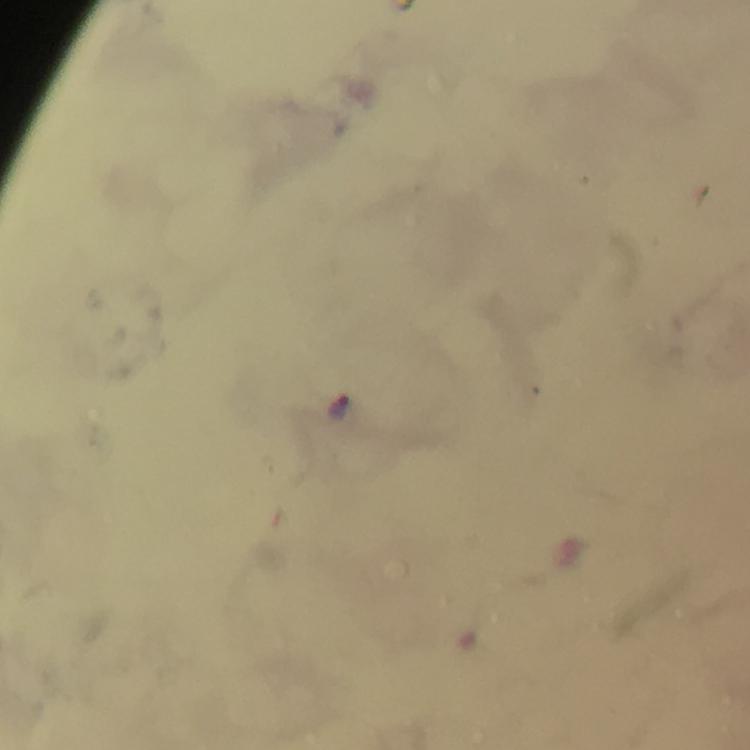

Approximate centers as [x, y] in pixels. Plasmodium parasite locations: [341, 405]. Cropped region of a single field of view. 100x magnification. Thick blood smear. Image is 750×750 pixels. Smartphone photograph taken through a microscope. From a malaria diagnostic workup. Giemsa stain. Immersion oil applied.